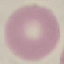 Malaria status: uninfected. Acquired by smartphone through the microscope eyepiece. Giemsa-stained preparation. Automatically extracted cell patch, resized to 64 × 64 pixels. Thin blood smear.